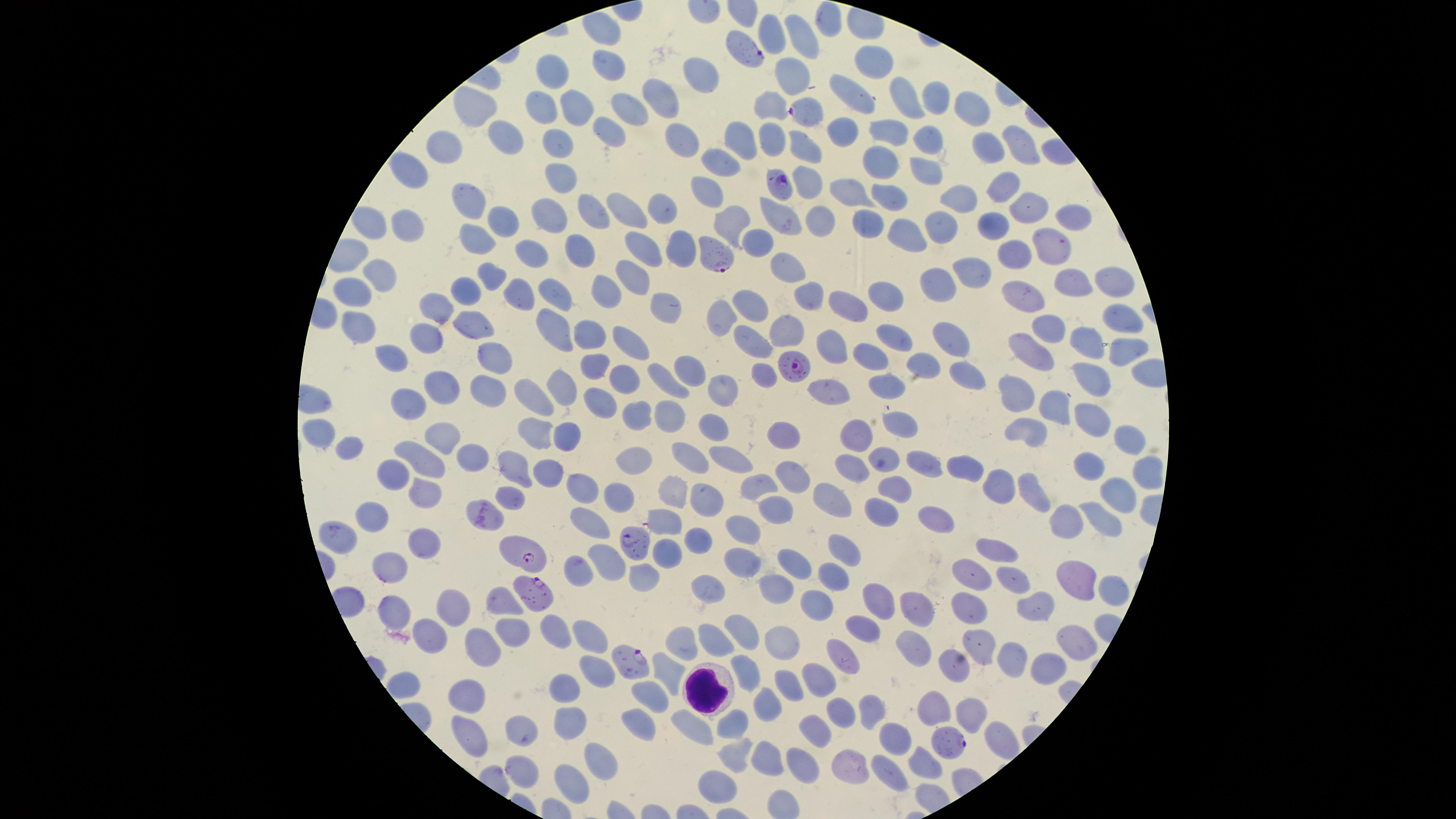
Approximate marker points as [x, y] in pixels. WBCs: [706, 687]. Uninfected RBCs: [831, 16], [770, 31], [809, 38], [871, 59], [617, 68], [786, 71], [556, 75], [705, 77], [851, 91], [659, 96], [935, 100], [911, 101], [576, 106], [479, 107], [625, 107], [546, 108], [772, 108], [976, 112], [845, 125], [612, 127], [898, 129], [506, 136], [744, 136], [779, 136], [925, 137], [681, 139], [556, 141], [1013, 144], [802, 145], [988, 145], [445, 150], [884, 156], [729, 158], [921, 166], [413, 168], [559, 172], [810, 182], [1007, 184], [706, 189], [841, 189], [894, 200], [970, 201], [474, 202], [630, 206], [666, 207], [1024, 207], [596, 208], [545, 212], [1069, 217], [502, 218], [736, 220], [782, 220], [815, 221], [987, 221], [413, 225], [871, 225], [943, 226], [902, 234], [482, 238], [758, 241], [651, 245], [532, 247], [1054, 247], [686, 248], [581, 251], [1015, 251], [791, 269], [632, 271], [976, 271], [490, 278], [382, 280], [1074, 281], [1107, 281], [937, 284], [606, 288], [519, 291], [467, 293], [556, 293], [360, 294], [890, 295], [806, 297], [1023, 299], [852, 300], [757, 302], [670, 306], [722, 311], [444, 312], [1123, 316], [555, 323], [365, 326], [476, 328], [1040, 328], [588, 332], [784, 332], [891, 335], [752, 337], [955, 339], [430, 340], [634, 340], [837, 345], [1081, 345], [1032, 348], [491, 352], [1120, 352], [395, 356], [879, 356], [920, 362], [599, 365], [960, 369], [687, 371], [765, 371], [1087, 373], [624, 379], [665, 383], [893, 384], [439, 386], [824, 388], [488, 389], [565, 389], [726, 389], [1011, 389], [530, 393], [597, 399], [1050, 403], [406, 408], [636, 414], [669, 415], [1092, 418], [710, 423], [902, 427], [1031, 427], [537, 431], [786, 435], [317, 436], [435, 436], [1126, 437], [566, 439], [856, 439], [354, 448], [420, 454], [884, 457], [729, 458], [641, 459], [685, 459], [1090, 460], [474, 462], [928, 464], [965, 465], [856, 469], [518, 470], [398, 473], [550, 473], [793, 475], [1000, 482], [892, 485], [1120, 485], [761, 486], [582, 488], [674, 490], [515, 491], [424, 492], [619, 492], [1031, 494], [705, 498], [837, 498], [775, 510], [878, 512], [372, 515], [670, 515], [934, 519], [1064, 519], [1098, 520], [593, 527], [744, 529], [335, 534], [698, 540], [851, 543], [998, 544], [419, 546], [668, 556], [607, 558], [742, 560], [800, 560], [384, 564], [579, 568], [641, 574], [831, 577], [972, 577], [1073, 579], [1016, 580], [711, 587], [1112, 588], [777, 590], [1029, 601], [502, 602], [874, 602], [813, 604], [452, 606], [972, 607], [916, 610], [394, 611], [864, 627], [552, 631], [511, 632], [590, 635], [746, 639], [785, 640], [685, 641], [717, 642], [911, 642], [1077, 642], [978, 648], [843, 650], [477, 653], [1014, 655], [956, 662], [1049, 665], [749, 669], [669, 671], [598, 673], [816, 679], [790, 684], [567, 691], [468, 694], [651, 698], [765, 701], [936, 706], [842, 708], [973, 712], [865, 714], [569, 717], [687, 719], [639, 720], [819, 723], [735, 727], [527, 732], [469, 734], [895, 743], [768, 756], [734, 757], [592, 758], [848, 761], [806, 763], [920, 763], [523, 767], [885, 774], [574, 778], [713, 785]. Parasitized RBCs: [748, 51], [809, 113], [779, 182], [715, 260], [788, 361], [639, 545], [519, 551], [531, 593], [633, 666], [946, 741]. Giemsa stain. Image is 1456×819 pixels. Species: Plasmodium falciparum. One field of view of the specimen. Presence: malaria parasites seen. Smartphone photograph through the microscope eyepiece. Thin blood film. The visible region is circular.